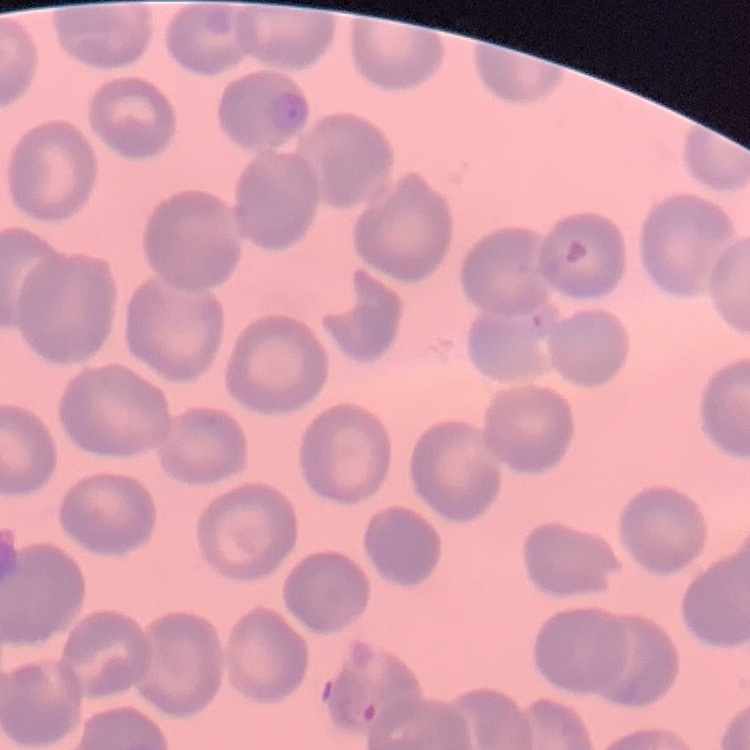
The red blood cells show no rouleaux formation. One tile cut from a larger photomicrograph. Thin blood smear. Field's or Giemsa stain.